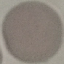 Result: no malaria parasites detected. Thin blood film. Giemsa stain. Photographed with a smartphone camera at the microscope eyepiece. Cell patch, automatically extracted from a larger field of view and resized to 64 × 64 pixels.